Assess for Plasmodium parasites.
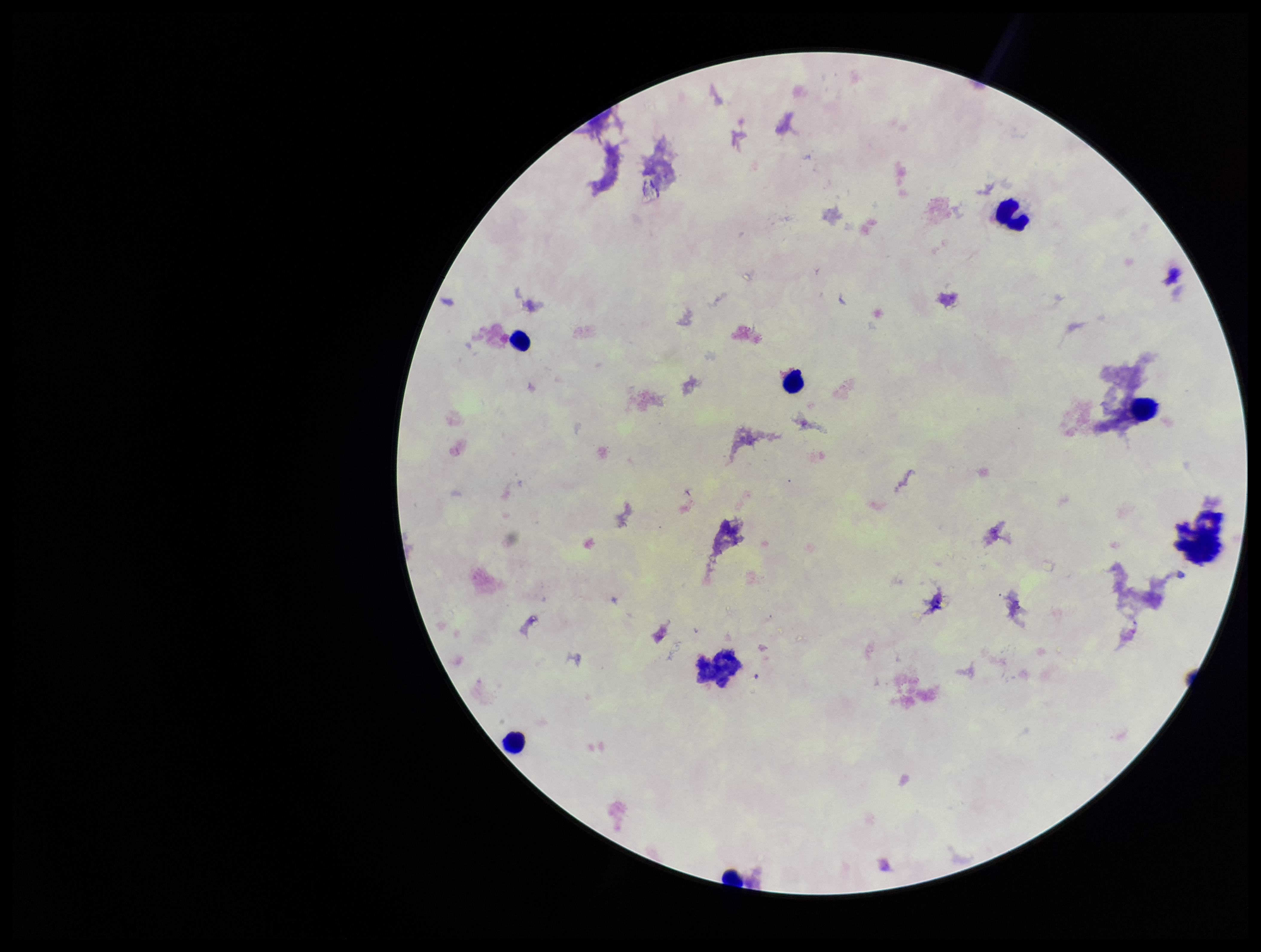

None detected.

Summary:
  - Capture: smartphone photograph through the microscope eyepiece
  - Stain: Giemsa
  - Image size: 1261×952 pixels
  - Field of view: single
  - Preparation: thick blood smear
  - Parasite count: 0
  - Leukocyte count: 6
  - Patient malaria status: negative